Classify this cell by malaria status.
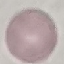
It is uninfected.

Summary:
  - Capture: smartphone through the microscope eyepiece
  - Stain: Giemsa
  - Image type: automatically extracted cell patch, resized to 64 × 64 pixels
  - Preparation: thin blood smear